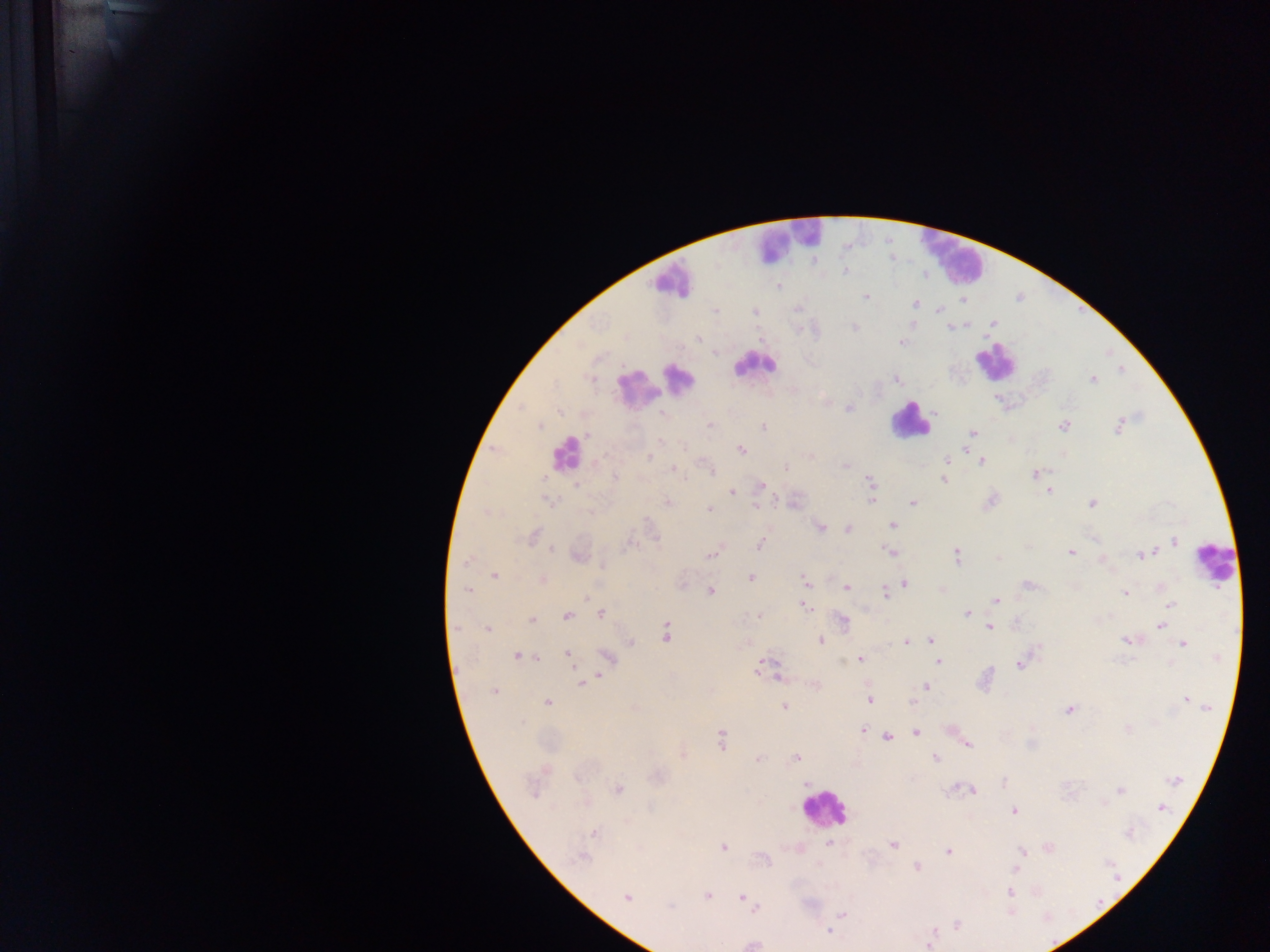

capture = mobile-phone photograph through a microscope
field of view = single
leukocyte locations = approximate centers as x y in pixels: 787 243; 956 254; 672 283; 997 359; 751 367; 681 376; 635 392; 912 419; 566 445; 1213 565; 826 812
preparation = thick blood smear
country = Ghana
malaria parasite locations = approximate centers as x y in pixels: 844 273; 866 297; 915 305; 938 310; 756 312; 853 328; 949 328; 698 337; 901 344; 601 355; 1122 369; 621 378; 896 378; 1091 380; 848 408; 558 411; 662 414; 1121 419; 708 423; 1064 425; 763 427; 1118 429; 547 430; 973 433; 589 434; 660 442; 684 444; 741 450; 649 457; 600 461; 945 462; 982 462; 845 464; 785 467; 672 469; 710 471; 1035 473; 615 477; 686 477; 544 479; 944 481; 869 483; 764 485; 576 488; 1050 490; 732 493; 872 494; 545 499; 548 500; 992 500; 778 501; 911 502; 1091 502; 668 503; 755 505; 710 510; 894 526; 820 528; 848 528; 533 536; 655 538; 1175 541; 629 544; 759 544; 552 549; 890 551; 1070 552; 1147 553; 957 555; 1139 555; 710 557; 997 557; 1102 559; 464 564; 601 568; 494 576; 751 578; 543 580; 806 582; 906 582; 682 583; 1027 584; 1159 585; 847 588; 468 591; 710 591; 1123 592; 885 593; 588 598; 995 600; 1168 604; 804 606; 601 614; 966 614; 567 615; 756 615; 532 620; 844 621; 1161 625; 988 627; 458 629; 488 630; 666 632; 930 640; 1124 640; 820 642; 630 643; 907 643; 1182 644; 567 655; 516 656; 522 656; 538 657; 861 659; 940 661; 843 662; 855 662; 761 664; 1020 664; 599 675; 777 677; 587 683; 581 684; 927 686; 493 690; 1185 699; 869 701; 910 702; 1198 702; 548 704; 1206 706; 784 707; 1068 710; 1128 729; 863 730; 916 733; 887 737; 722 740; 967 744; 683 755; 758 757; 798 757; 935 758; 1178 780; 1004 781; 951 788; 618 789; 973 790; 1120 790; 1104 805; 1165 809; 1013 813; 594 833; 829 843; 894 845; 1048 847; 722 848; 947 851; 1022 851; 580 860; 762 860; 916 865; 1016 872; 1011 891; 706 895; 626 898; 741 898; 670 907; 755 908; 841 914; 1046 915; 957 923; 830 932; 933 935; 752 945
image size = 1270×952 pixels